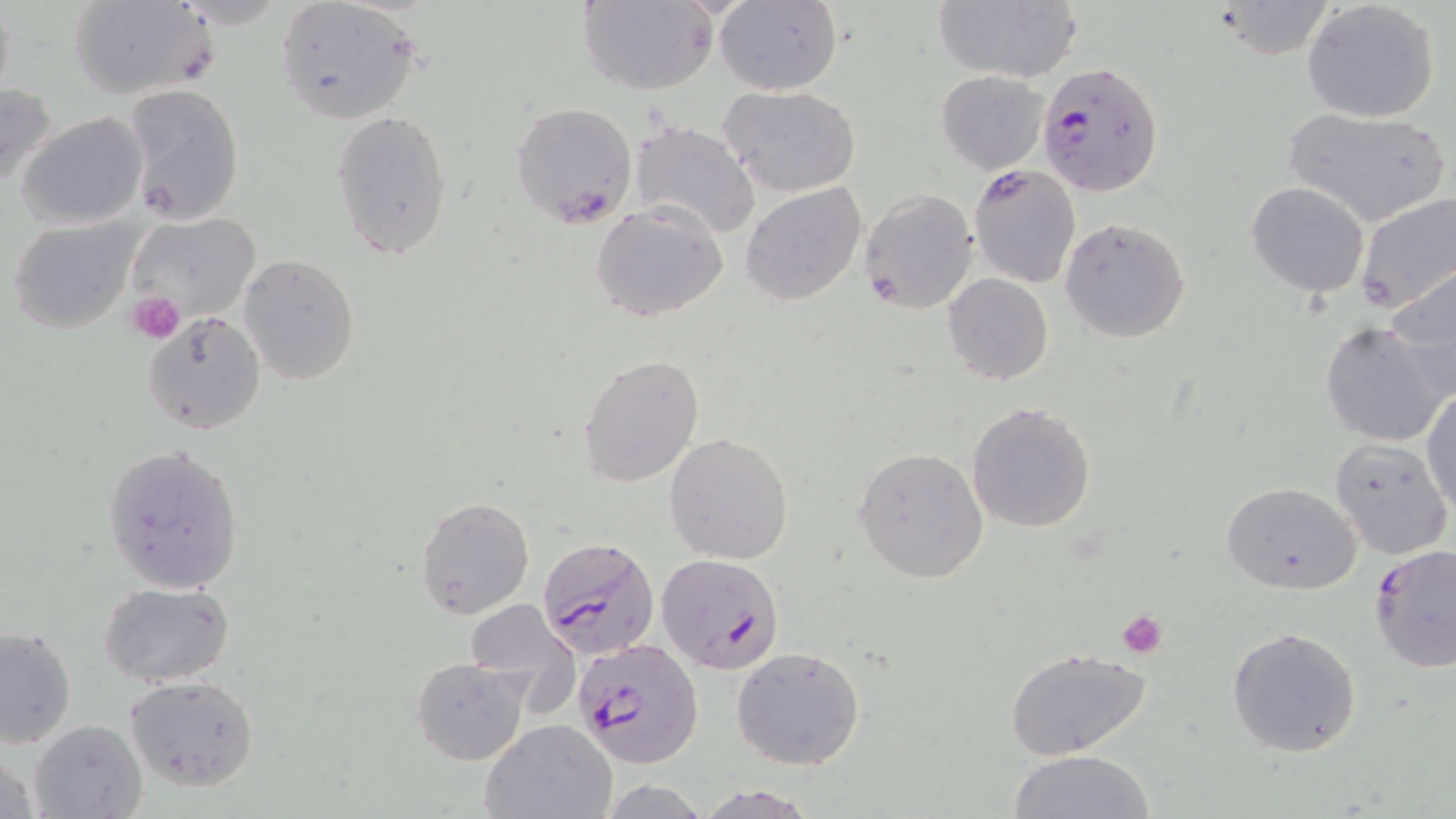
Summary:
  - Coordinate format: approximate bounding boxes as (x1,y1)-(x2,y2) corner pairs in pixels
  - Platelet locations: (127,290)-(186,343), (1116,609)-(1167,658)
  - Plasmodium falciparum-infected red blood cell locations: (1037,60)-(1165,196), (969,164)-(1081,287), (538,538)-(661,660), (1369,543)-(1456,672), (655,552)-(784,674), (574,640)-(706,769)
  - Uninfected red blood cell locations: (67,0)-(219,102), (577,0)-(719,95), (715,0)-(840,96), (934,0)-(1080,83), (1301,0)-(1441,123), (278,1)-(420,125), (1213,2)-(1338,59), (936,70)-(1049,174), (0,81)-(58,195), (122,85)-(245,223), (720,85)-(862,198), (511,101)-(637,229), (331,106)-(453,259), (1281,108)-(1450,227), (17,110)-(148,231), (629,119)-(762,241), (740,182)-(868,305), (1246,182)-(1370,298), (859,189)-(978,313), (1354,191)-(1456,315), (591,201)-(728,322), (123,213)-(261,329), (8,216)-(141,334), (1060,219)-(1191,343), (238,254)-(361,387), (1384,265)-(1456,395), (942,274)-(1053,386), (143,311)-(265,434), (1319,322)-(1450,447), (578,354)-(705,488), (1421,386)-(1455,514), (966,408)-(1101,534), (665,433)-(795,565), (1330,436)-(1453,560), (103,443)-(246,594), (852,446)-(987,581), (1221,482)-(1362,594), (415,497)-(534,619), (101,580)-(236,687), (464,599)-(580,703), (1,625)-(76,748), (1228,626)-(1362,758), (732,645)-(866,771), (1004,647)-(1153,759), (410,658)-(529,764), (126,674)-(259,792), (31,718)-(147,819), (480,719)-(617,819), (1008,749)-(1157,819), (691,785)-(821,818)
  - Slide-level diagnosis: Plasmodium falciparum
  - Stain: May-Grünwald-Giemsa
  - Preparation: thin blood smear
  - Modality: optical microscopy
  - Magnification: 1000x
  - Field of view: one of a larger specimen
  - Image size: 1456×819 pixels